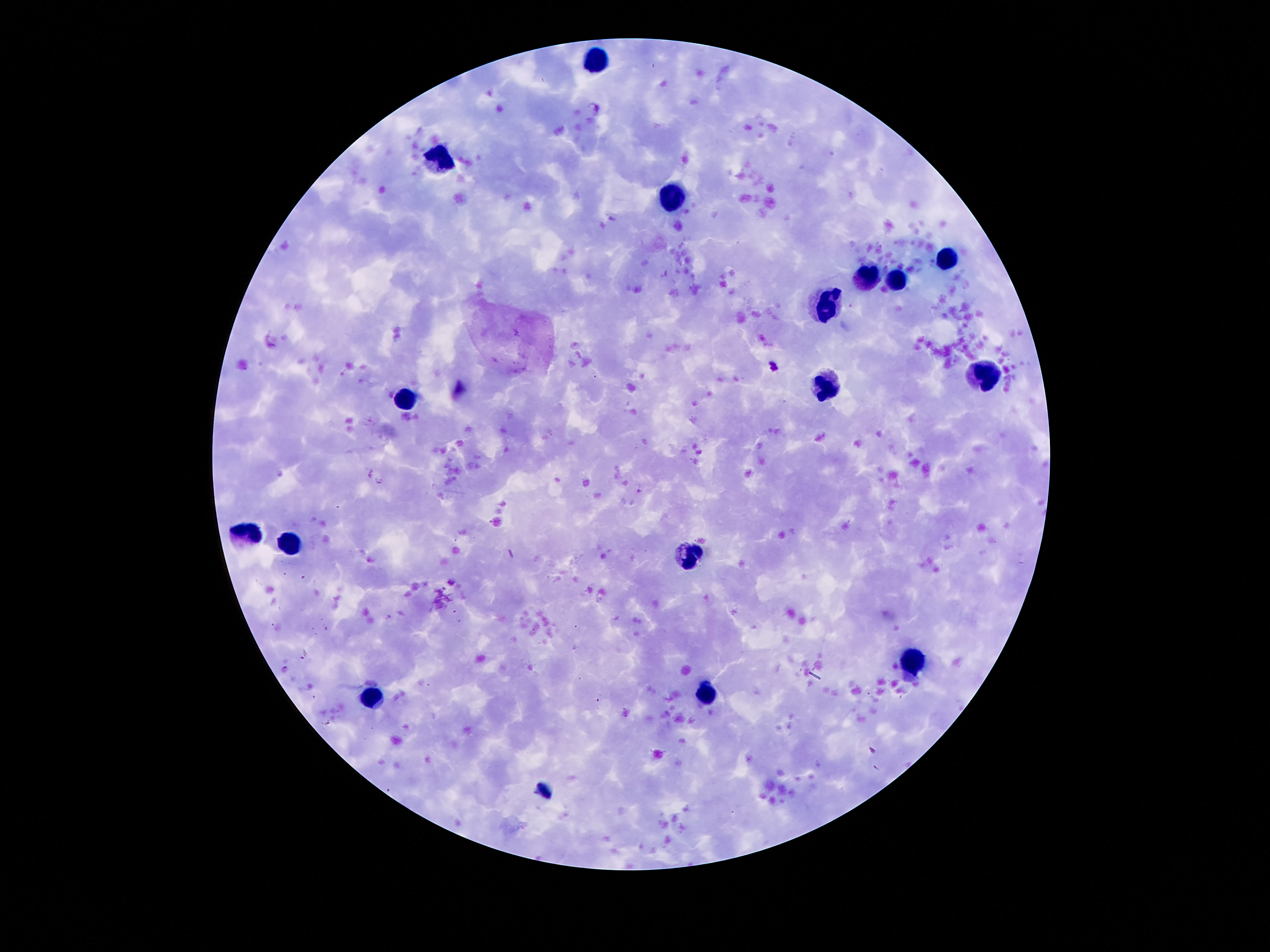
Approximate centers as (x, y) in pixels.
Summary:
  - Leukocyte locations: (594, 55), (440, 162), (673, 204), (951, 256), (867, 277), (898, 283), (827, 302), (991, 378), (827, 384), (407, 401), (243, 531), (291, 542), (692, 556), (913, 663), (707, 695), (373, 699)
  - Capture: smartphone camera through the microscope eyepiece
  - Field of view: single
  - Patient malaria status: negative
  - Magnification: 100x
  - Preparation: thick blood film
  - Stain: Giemsa
  - Image size: 1270×952 pixels